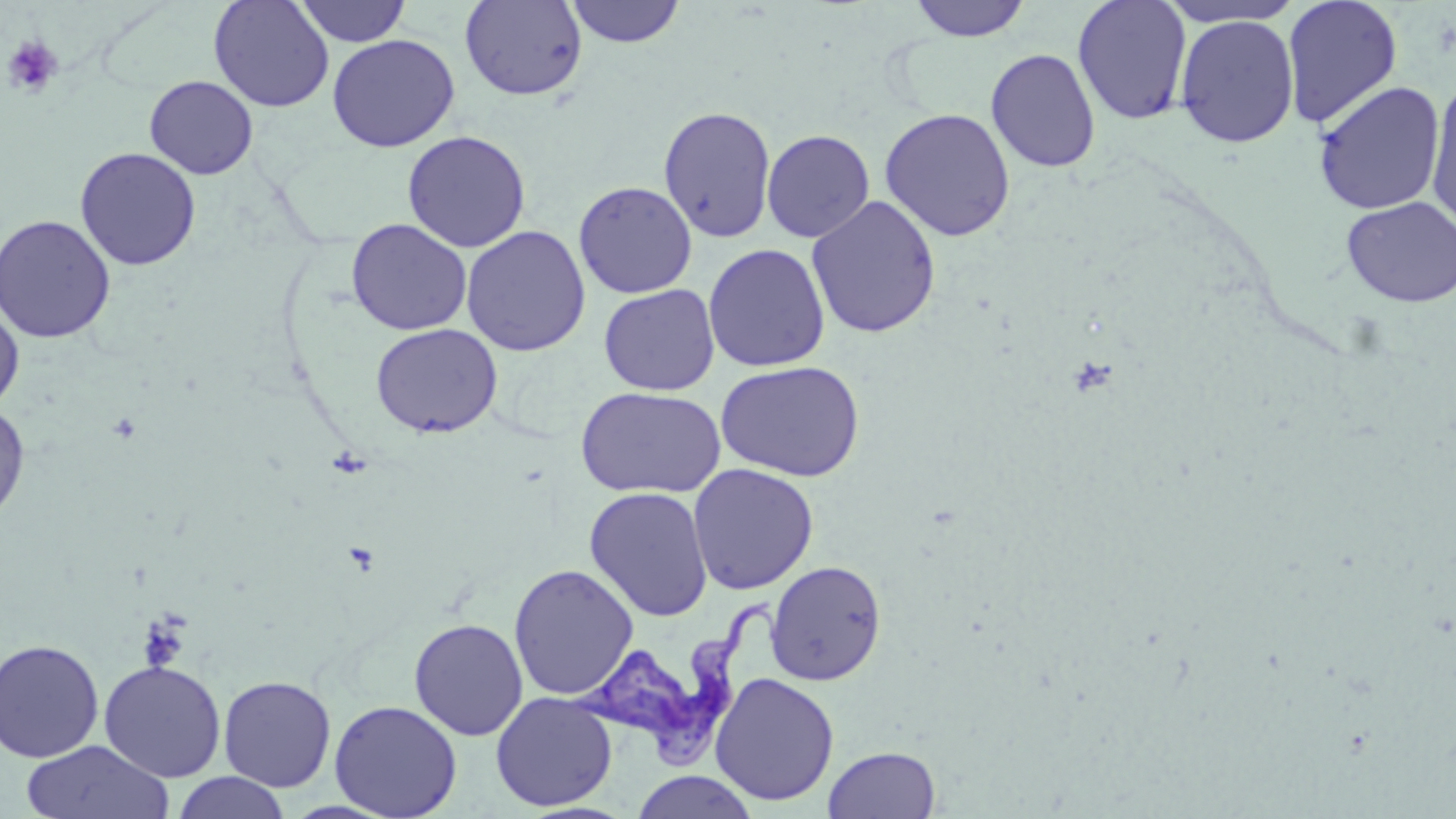

Summary:
  - Coordinate format: approximate bounding boxes as (x1, y1, x2, y2) in pixels
  - Trypanosoma brucei locations: (571, 596, 781, 769)
  - Uninfected red blood cell locations: (208, 0, 334, 113), (459, 0, 588, 101), (907, 0, 1032, 42), (1072, 0, 1193, 125), (1159, 0, 1303, 30), (1281, 0, 1403, 128), (294, 1, 410, 47), (564, 1, 687, 48), (1174, 13, 1300, 147), (327, 34, 460, 152), (985, 48, 1101, 173), (144, 75, 258, 179), (1312, 81, 1445, 215), (1425, 81, 1456, 231), (657, 105, 777, 243), (879, 107, 1016, 242), (761, 129, 875, 243), (402, 130, 531, 253), (75, 147, 201, 271), (573, 180, 697, 299), (806, 195, 942, 339), (1341, 196, 1456, 308), (0, 213, 116, 344), (346, 218, 472, 336), (461, 225, 591, 356), (703, 243, 830, 372), (599, 284, 720, 396), (0, 299, 24, 414), (370, 323, 503, 438), (715, 360, 865, 482), (575, 386, 725, 499), (0, 401, 30, 526), (687, 463, 819, 595), (584, 486, 713, 622), (766, 560, 887, 686), (508, 563, 639, 700), (408, 618, 529, 741), (0, 638, 105, 763), (98, 660, 226, 782), (710, 671, 839, 806), (217, 675, 337, 792), (490, 691, 618, 811), (329, 699, 463, 818), (21, 740, 175, 819), (823, 745, 941, 819), (630, 771, 759, 819), (172, 772, 290, 818)
  - Platelet locations: (1, 34, 64, 98), (137, 614, 190, 672)
  - Slide-level diagnosis: Trypanosoma brucei
  - Stain: May-Grünwald-Giemsa
  - Magnification: 1000x
  - Preparation: thin blood smear
  - Image size: 1456×819 pixels
  - Modality: optical microscopy
  - Field of view: single